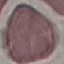 Malaria status: uninfected. Acquired by smartphone through the microscope eyepiece. Thin blood film. Cell patch, automatically extracted from a larger field of view and resized to 64 × 64 pixels. Giemsa stain.